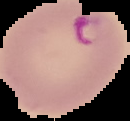

Summary:
  - Image size: 130×121 pixels
  - Malaria status: parasitized
  - Preparation: thin blood smear
  - Image type: cell region segmented out of the field of view; surrounding area masked to black